Describe the morphology of the red blood cells.
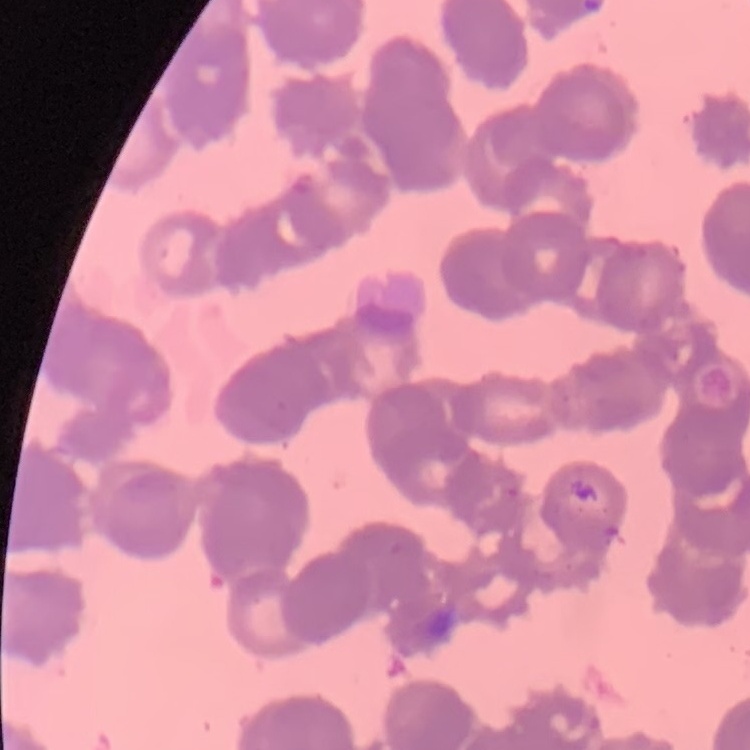

Rouleaux formation.

Summary:
  - Stain: Field's or Giemsa
  - Preparation: thin peripheral smear
  - Image type: square crop of a larger photomicrograph